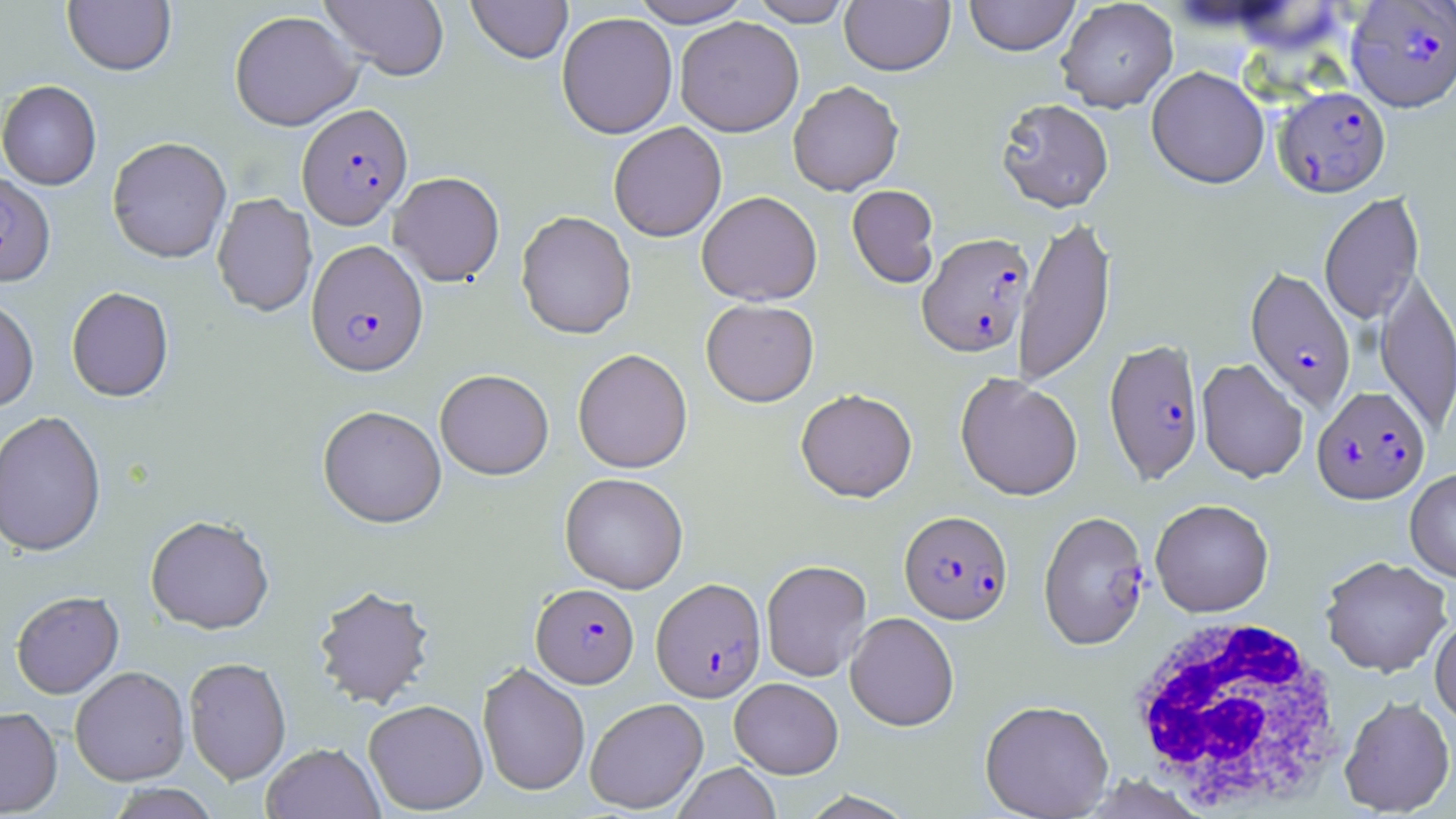

Summary:
  - Coordinate format: approximate bounding boxes as [x1, y1, x2, y2] in pixels
  - White blood cell locations: [1124, 614, 1348, 814]
  - Uninfected red blood cell locations: [63, 0, 176, 77], [319, 0, 449, 80], [466, 0, 573, 64], [629, 0, 753, 27], [747, 0, 854, 26], [840, 0, 955, 76], [964, 0, 1080, 57], [1056, 0, 1178, 113], [229, 10, 363, 131], [556, 11, 678, 139], [674, 17, 804, 137], [1146, 67, 1269, 190], [0, 80, 102, 190], [788, 80, 904, 196], [995, 98, 1114, 214], [608, 122, 727, 242], [107, 137, 232, 264], [389, 172, 505, 286], [847, 185, 940, 288], [696, 191, 822, 306], [1319, 192, 1424, 326], [212, 193, 317, 317], [516, 210, 636, 339], [1013, 212, 1115, 387], [1375, 270, 1456, 437], [66, 287, 174, 403], [0, 298, 39, 413], [701, 298, 819, 407], [572, 349, 692, 473], [1196, 358, 1308, 483], [435, 369, 554, 480], [955, 372, 1083, 501], [795, 388, 918, 502], [317, 405, 447, 528], [0, 411, 107, 558], [1405, 469, 1456, 582], [560, 472, 688, 593], [1150, 499, 1274, 617], [145, 515, 274, 635], [1320, 556, 1453, 677], [761, 559, 872, 681], [312, 584, 436, 710], [11, 592, 124, 700], [845, 612, 959, 731], [1430, 617, 1456, 725], [184, 657, 291, 785], [477, 662, 590, 797], [69, 667, 191, 785], [729, 677, 843, 778], [1339, 696, 1456, 817], [585, 697, 708, 814], [363, 699, 488, 815], [979, 700, 1114, 818], [0, 707, 62, 816], [261, 743, 384, 819], [673, 762, 781, 818], [105, 784, 221, 819]
  - Plasmodium falciparum-infected red blood cell locations: [1345, 1, 1456, 116], [1273, 88, 1391, 199], [297, 103, 413, 229], [0, 172, 56, 288], [917, 232, 1035, 358], [306, 239, 429, 377], [1244, 267, 1357, 414], [1104, 338, 1205, 485], [1312, 386, 1432, 506], [899, 510, 1013, 625], [1039, 510, 1150, 650], [651, 577, 766, 702], [531, 583, 639, 688]
  - Slide-level diagnosis: Plasmodium falciparum
  - Modality: light microscopy
  - Stain: May-Grünwald-Giemsa
  - Image size: 1456×819 pixels
  - Magnification: 1000x
  - Preparation: thin blood smear
  - Field of view: single